Outline each uninfected red blood cell.
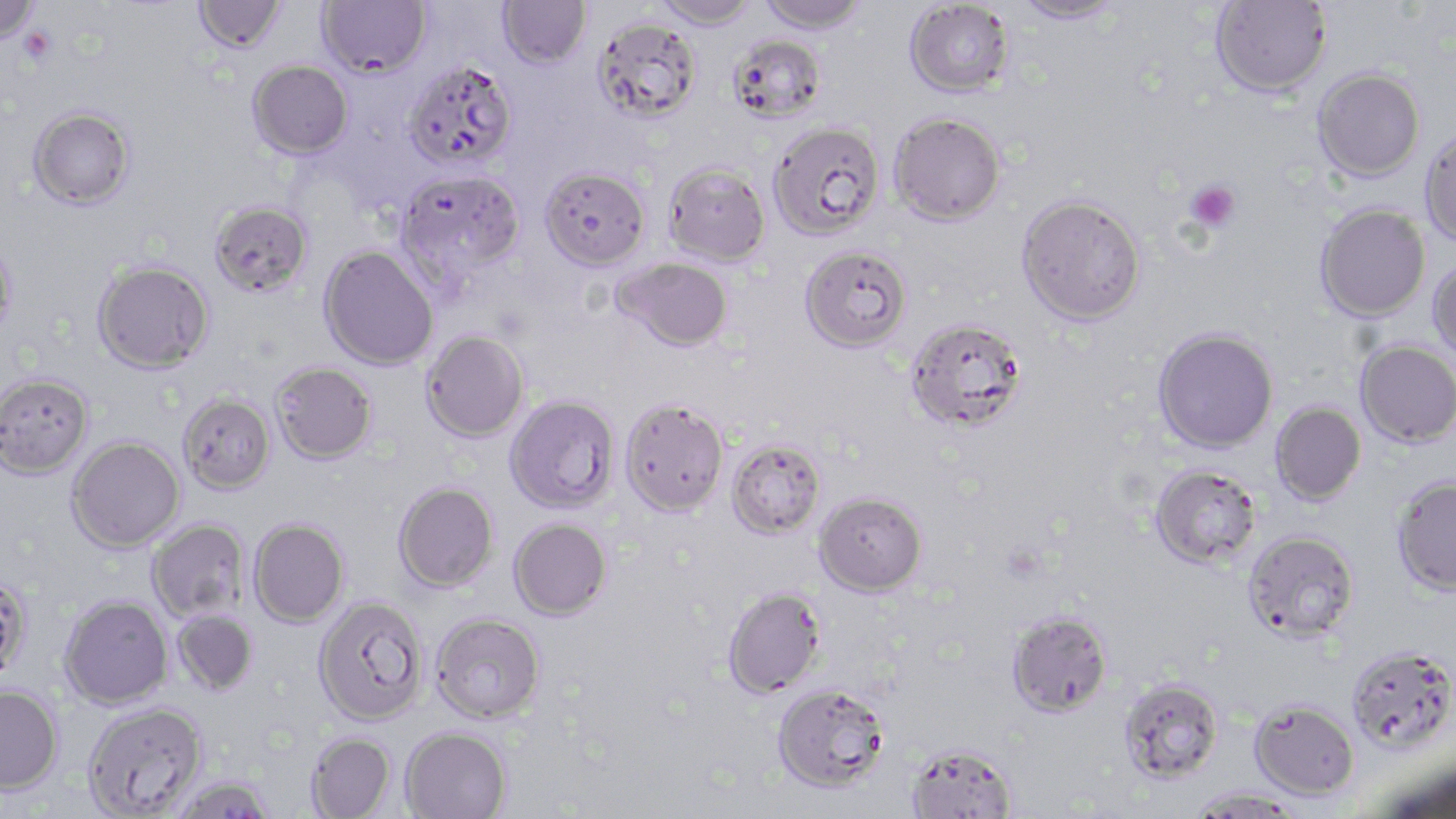
Approximate bounding boxes as named x1/y1/x2/y2 corners in pixels.
Uninfected red blood cells: (x1=0, y1=0, x2=41, y2=48), (x1=193, y1=0, x2=287, y2=54), (x1=317, y1=0, x2=432, y2=78), (x1=497, y1=0, x2=591, y2=70), (x1=651, y1=0, x2=759, y2=30), (x1=756, y1=0, x2=870, y2=34), (x1=904, y1=0, x2=1015, y2=98), (x1=1011, y1=0, x2=1128, y2=25), (x1=1210, y1=0, x2=1332, y2=97), (x1=592, y1=17, x2=702, y2=124), (x1=729, y1=34, x2=827, y2=123), (x1=247, y1=59, x2=353, y2=159), (x1=404, y1=60, x2=518, y2=172), (x1=1312, y1=67, x2=1425, y2=181), (x1=27, y1=106, x2=136, y2=210), (x1=888, y1=111, x2=1006, y2=226), (x1=768, y1=121, x2=885, y2=242), (x1=1419, y1=127, x2=1456, y2=247), (x1=664, y1=162, x2=770, y2=266), (x1=539, y1=165, x2=650, y2=269), (x1=397, y1=169, x2=525, y2=283), (x1=1016, y1=194, x2=1146, y2=326), (x1=209, y1=200, x2=312, y2=298), (x1=1315, y1=204, x2=1430, y2=322), (x1=0, y1=236, x2=17, y2=345), (x1=319, y1=245, x2=439, y2=370), (x1=799, y1=245, x2=912, y2=353), (x1=612, y1=256, x2=733, y2=353), (x1=1428, y1=257, x2=1456, y2=362), (x1=92, y1=260, x2=215, y2=374), (x1=905, y1=318, x2=1028, y2=433), (x1=1152, y1=327, x2=1278, y2=454), (x1=420, y1=330, x2=529, y2=443), (x1=1355, y1=340, x2=1456, y2=448), (x1=270, y1=361, x2=377, y2=465), (x1=0, y1=372, x2=93, y2=479), (x1=176, y1=392, x2=275, y2=495), (x1=504, y1=394, x2=620, y2=514), (x1=619, y1=398, x2=729, y2=516), (x1=1269, y1=401, x2=1366, y2=506), (x1=66, y1=436, x2=185, y2=553), (x1=726, y1=438, x2=827, y2=539), (x1=1149, y1=464, x2=1263, y2=569), (x1=1391, y1=475, x2=1456, y2=596), (x1=393, y1=481, x2=499, y2=592), (x1=814, y1=490, x2=928, y2=596), (x1=509, y1=517, x2=612, y2=620), (x1=248, y1=518, x2=349, y2=627), (x1=147, y1=519, x2=251, y2=623), (x1=1242, y1=530, x2=1360, y2=641), (x1=0, y1=572, x2=33, y2=683), (x1=722, y1=586, x2=826, y2=698), (x1=59, y1=595, x2=172, y2=709), (x1=313, y1=595, x2=428, y2=725), (x1=1006, y1=609, x2=1112, y2=718), (x1=172, y1=610, x2=259, y2=695), (x1=430, y1=612, x2=545, y2=724), (x1=1346, y1=645, x2=1456, y2=754), (x1=1119, y1=678, x2=1225, y2=783), (x1=772, y1=683, x2=891, y2=793), (x1=0, y1=685, x2=63, y2=794), (x1=1249, y1=699, x2=1360, y2=799), (x1=82, y1=702, x2=208, y2=818), (x1=400, y1=726, x2=512, y2=818), (x1=306, y1=732, x2=396, y2=818), (x1=906, y1=742, x2=1018, y2=818), (x1=1377, y1=759, x2=1456, y2=818), (x1=169, y1=775, x2=278, y2=819), (x1=1188, y1=787, x2=1307, y2=817).

Platelet locations: (x1=17, y1=26, x2=55, y2=64), (x1=1185, y1=178, x2=1241, y2=233). Slide-level diagnosis: Plasmodium falciparum. Image is 1456×819 pixels. Thin blood smear. May-Grünwald-Giemsa stain. Light microscopy. One field of a larger specimen. Captured at 1000x magnification.